Comment on the morphology of the red blood cells.
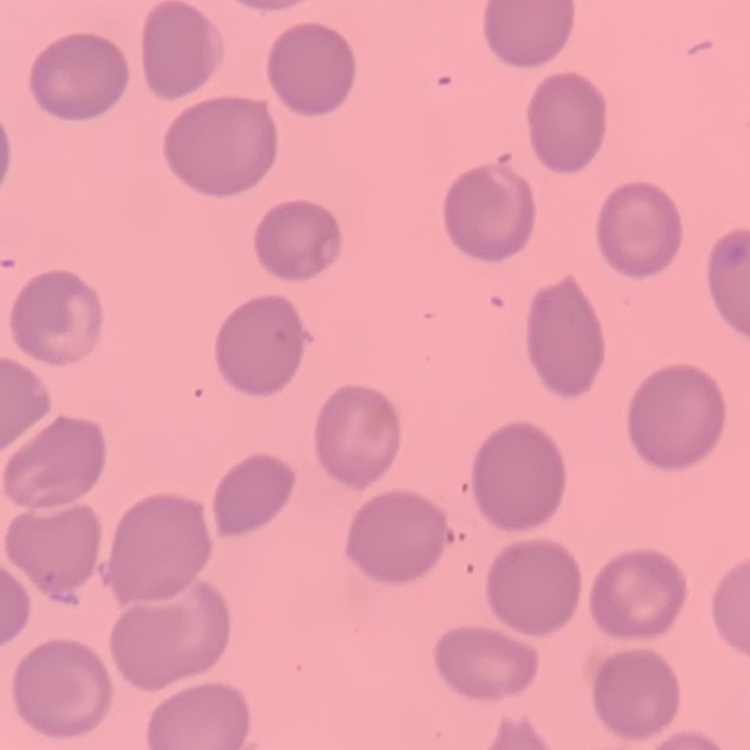
They show no rouleaux formation.

One tile cut from a larger photomicrograph. Stained with either Field's or Giemsa. Thin blood film.